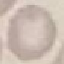
Malaria status: uninfected. Thin blood smear. Acquired by smartphone through the microscope eyepiece. Automatically extracted cell patch, resized to 64 × 64 pixels. Giemsa-stained preparation.